Assess the morphology of the erythrocytes.
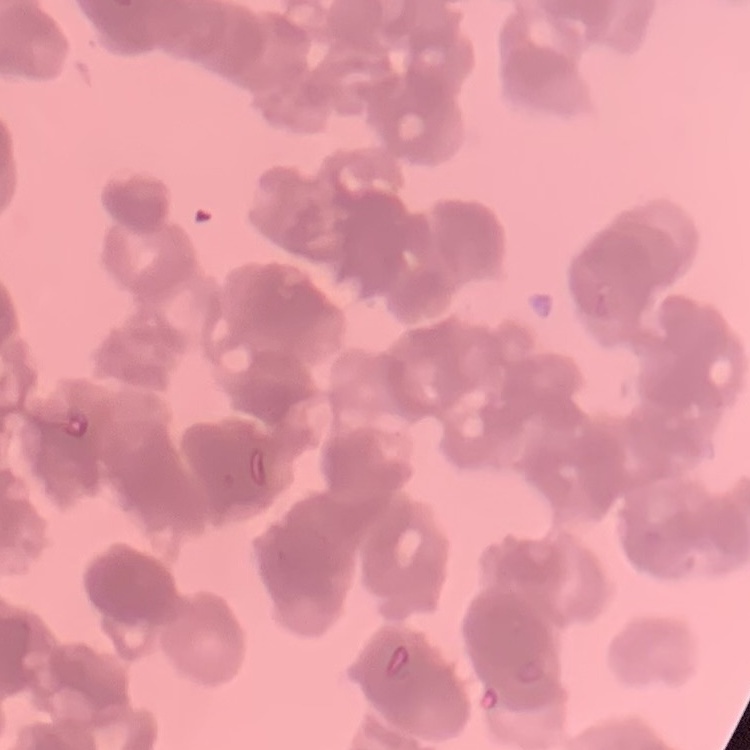
They show rouleaux formation.

preparation = thin blood smear
stain = Field's or Giemsa
image type = one tile cut from a larger photomicrograph